Report the malaria status of this cell.
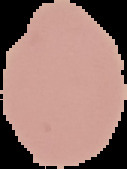

Uninfected.

Image is 127×169 pixels. Segmented cell region on a black background. From a thin blood film.